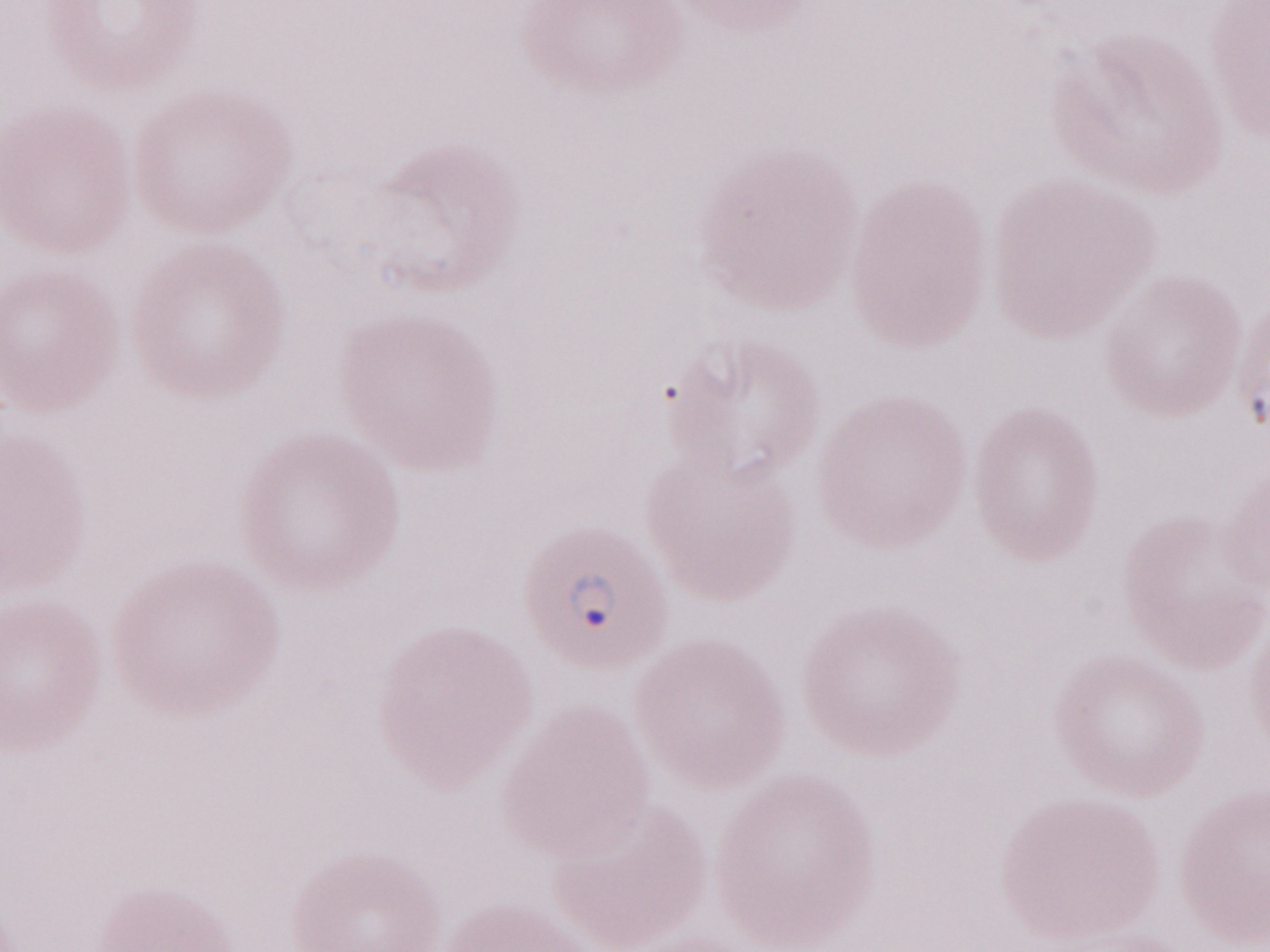 Olympus BX43 microscope and DP73 digital camera. Magnification: 1,000x. Single field of view. Image is 1270×952 pixels. Patient-level malaria diagnosis: positive. May-Grünwald-Giemsa stain. Thin blood smear.